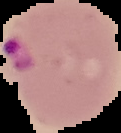

result = Plasmodium parasites identified
image type = cell region segmented out of the field of view; surrounding area masked to black
image size = 121×133 pixels
preparation = thin blood film